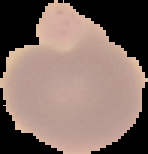

preparation: thin blood smear
image_type: cell region segmented out of the field of view; surrounding area masked to black
image_size: 148×154 pixels
malaria_status: uninfected